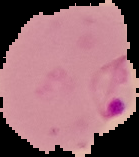
image type = segmented cell region on a black background
malaria status = parasitized
preparation = thin blood film
image size = 139×157 pixels